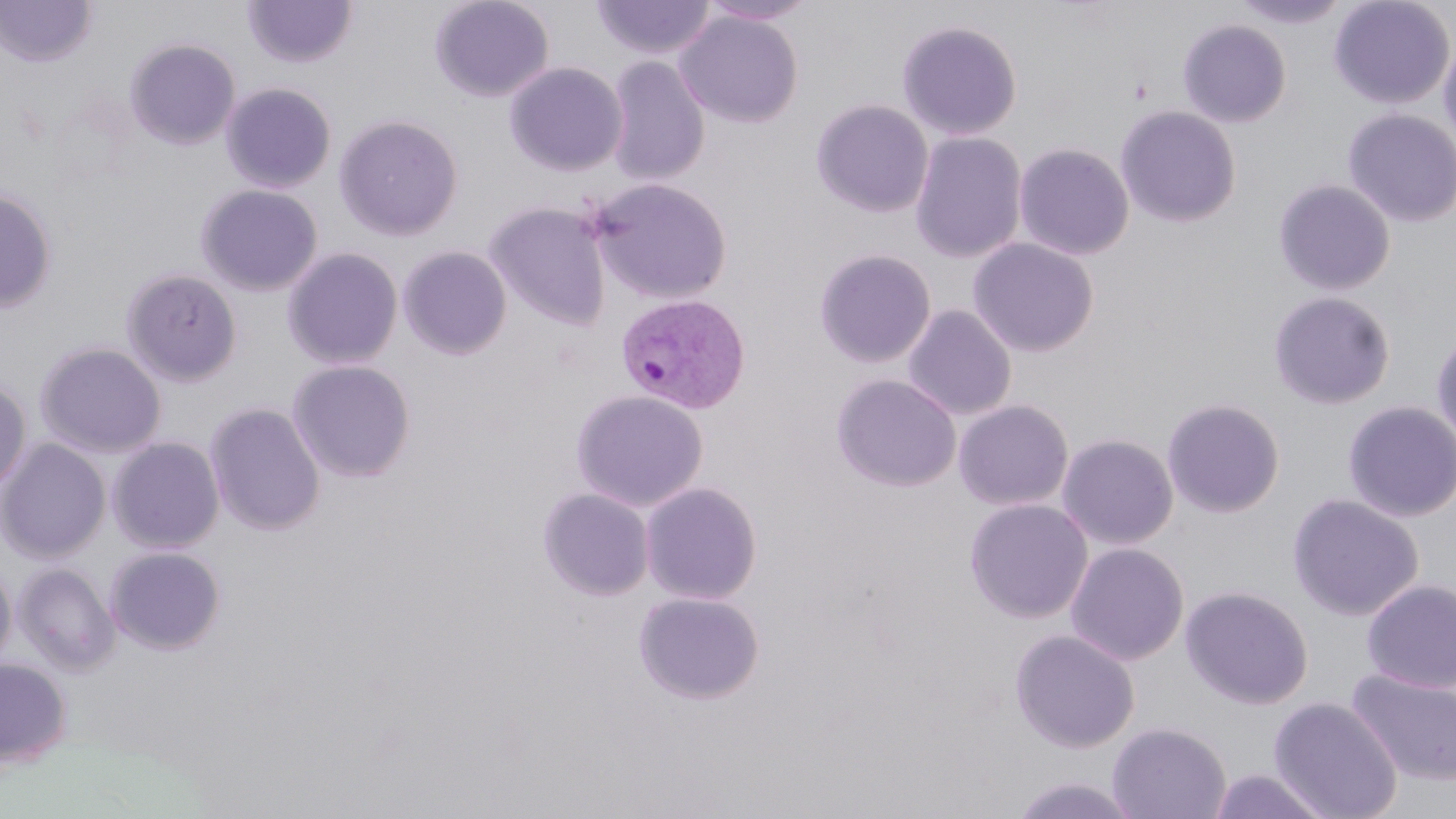
Summary:
  - Coordinate format: approximate bounding boxes as (x1, y1, x2, y2) in pixels
  - Uninfected red blood cell locations: (243, 0, 358, 68), (429, 0, 554, 102), (592, 0, 716, 60), (699, 0, 820, 25), (1230, 0, 1351, 28), (1328, 0, 1455, 109), (0, 1, 97, 68), (675, 10, 804, 128), (896, 19, 1023, 140), (1177, 19, 1291, 127), (1438, 34, 1456, 155), (124, 38, 240, 150), (605, 55, 711, 186), (504, 61, 628, 176), (221, 82, 337, 193), (811, 98, 934, 218), (1116, 106, 1241, 227), (1342, 109, 1456, 227), (334, 114, 464, 241), (910, 132, 1027, 263), (1014, 142, 1135, 260), (587, 178, 733, 304), (1273, 179, 1396, 295), (196, 184, 323, 296), (0, 188, 57, 313), (485, 201, 611, 330), (967, 237, 1100, 357), (398, 245, 512, 360), (282, 247, 404, 369), (814, 248, 936, 368), (121, 268, 242, 386), (1267, 290, 1396, 409), (903, 304, 1017, 420), (1431, 326, 1456, 452), (35, 341, 167, 458), (288, 359, 416, 483), (830, 374, 961, 492), (0, 376, 32, 494), (570, 389, 709, 512), (1161, 397, 1285, 518), (953, 399, 1074, 511), (1342, 400, 1456, 522), (205, 402, 325, 535), (1057, 433, 1179, 550), (108, 436, 225, 553), (0, 438, 111, 564), (641, 481, 763, 604), (538, 488, 655, 601), (1287, 493, 1424, 621), (964, 498, 1094, 623), (1066, 542, 1189, 665), (105, 547, 226, 654), (0, 559, 16, 672), (13, 562, 120, 674), (1361, 579, 1456, 694), (1180, 585, 1314, 709), (633, 590, 765, 704), (1009, 629, 1140, 753), (0, 658, 72, 769), (1346, 668, 1456, 787), (1269, 696, 1403, 819), (1107, 722, 1232, 819), (1207, 768, 1332, 818), (1009, 775, 1140, 818)
  - Plasmodium vivax-infected red blood cell locations: (615, 293, 751, 414)
  - Slide-level diagnosis: Plasmodium vivax
  - Image size: 1456×819 pixels
  - Preparation: thin blood film
  - Modality: optical microscopy
  - Magnification: 1000x
  - Field of view: single
  - Stain: May-Grünwald-Giemsa